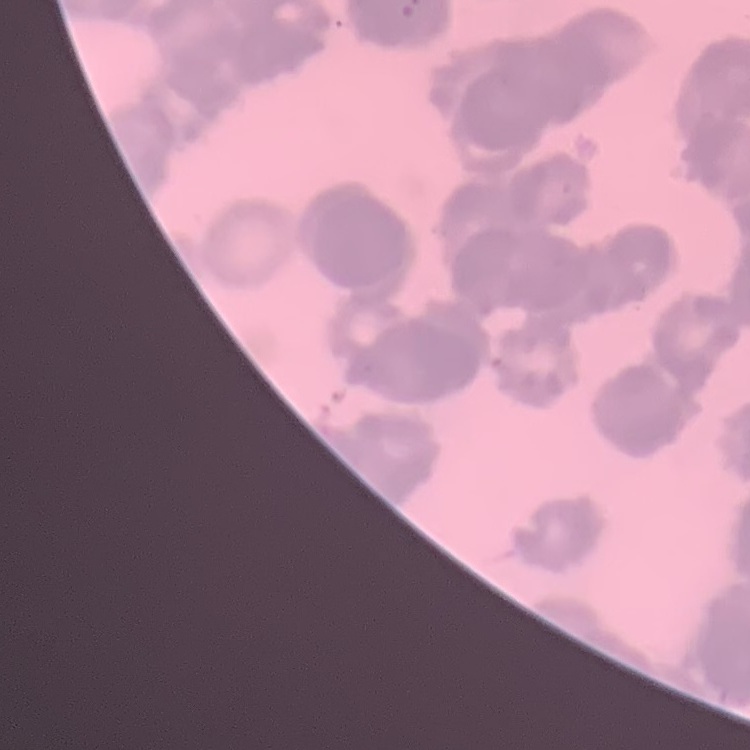
The red blood cells show rouleaux formation. Thin blood film. Stained with either Field's or Giemsa. One tile cut from a larger photomicrograph.